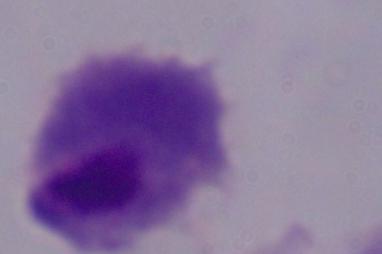

magnification = 1000x
modality = micrograph
identification = trichomonad